Assess this cell for malaria.
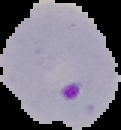
It is parasitized.

preparation: thin blood smear
image_type: segmented cell region on a black background
image_size: 121×130 pixels